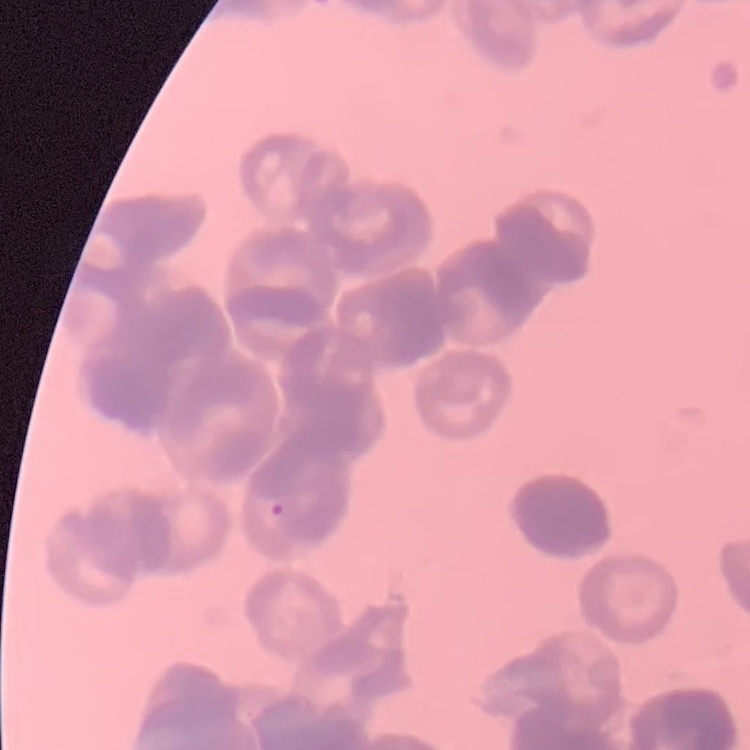

Summary:
  - Red blood cell morphology: rouleaux formation
  - Preparation: thin peripheral smear
  - Image type: square crop of a larger photomicrograph
  - Stain: Field's or Giemsa